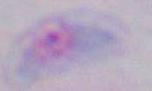
identification = Toxoplasma gondii
modality = micrograph
magnification = 1000x